Identify the parasite.
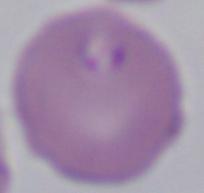

This is Babesia.

1000x magnification. Micrograph.